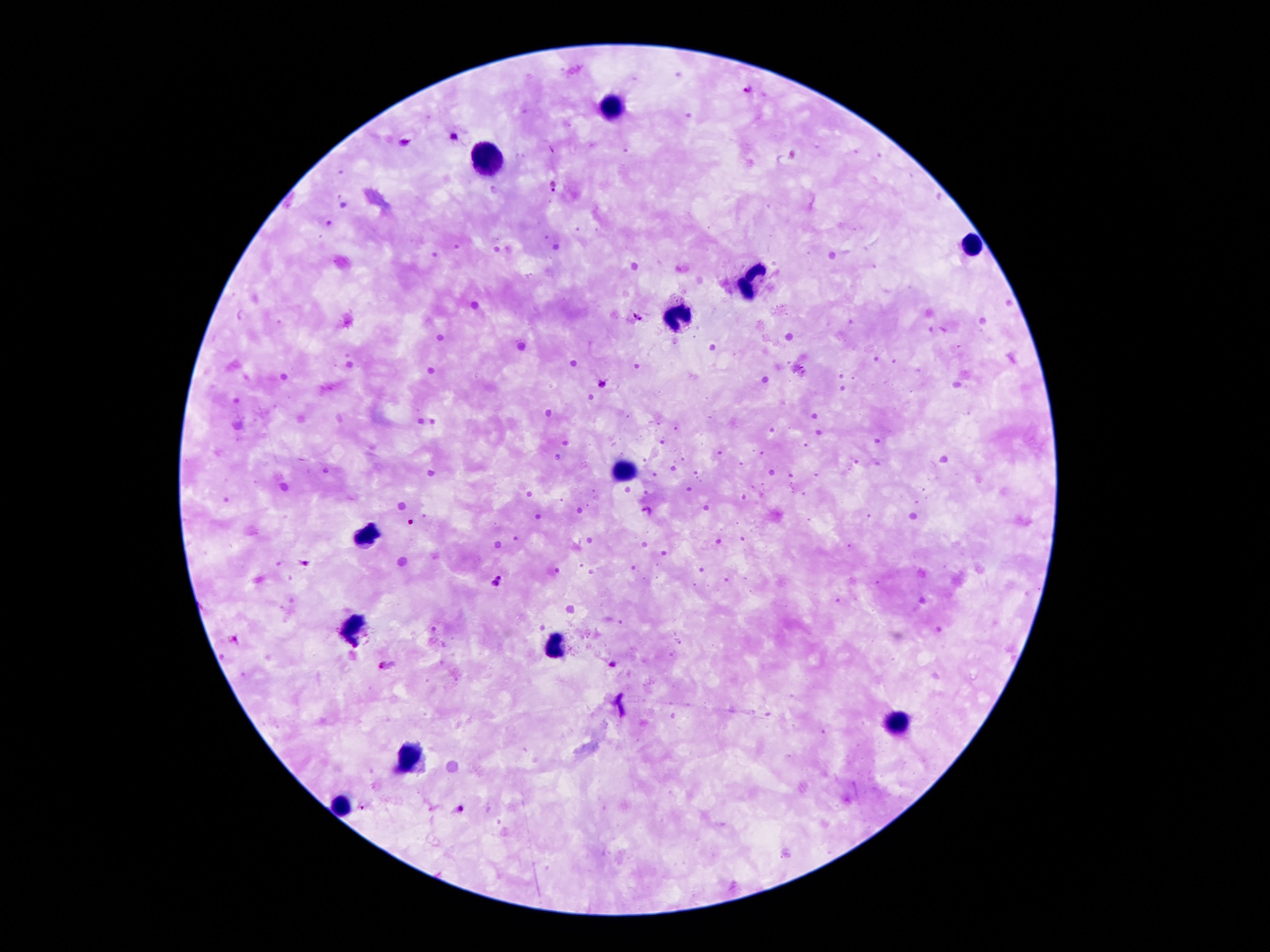

{
  "leukocyte_locations": "approximate centers as {x, y} in pixels: {613, 108}, {484, 158}, {972, 246}, {753, 279}, {680, 319}, {623, 470}, {367, 532}, {352, 625}, {554, 650}, {898, 728}, {409, 756}, {342, 806}",
  "magnification": "100x",
  "field_of_view": "single",
  "patient_malaria_status": "positive for Plasmodium falciparum",
  "image_size": "1270×952 pixels",
  "plasmodium_parasite_locations": "approximate centers as {x, y} in pixels: {747, 89}, {455, 138}, {554, 185}, {637, 316}, {602, 383}, {647, 511}, {411, 523}, {306, 564}, {499, 576}, {495, 584}, {614, 664}, {387, 666}, {461, 808}, {362, 809}",
  "stain": "Giemsa",
  "capture": "smartphone camera through the microscope eyepiece",
  "preparation": "thick blood film"
}